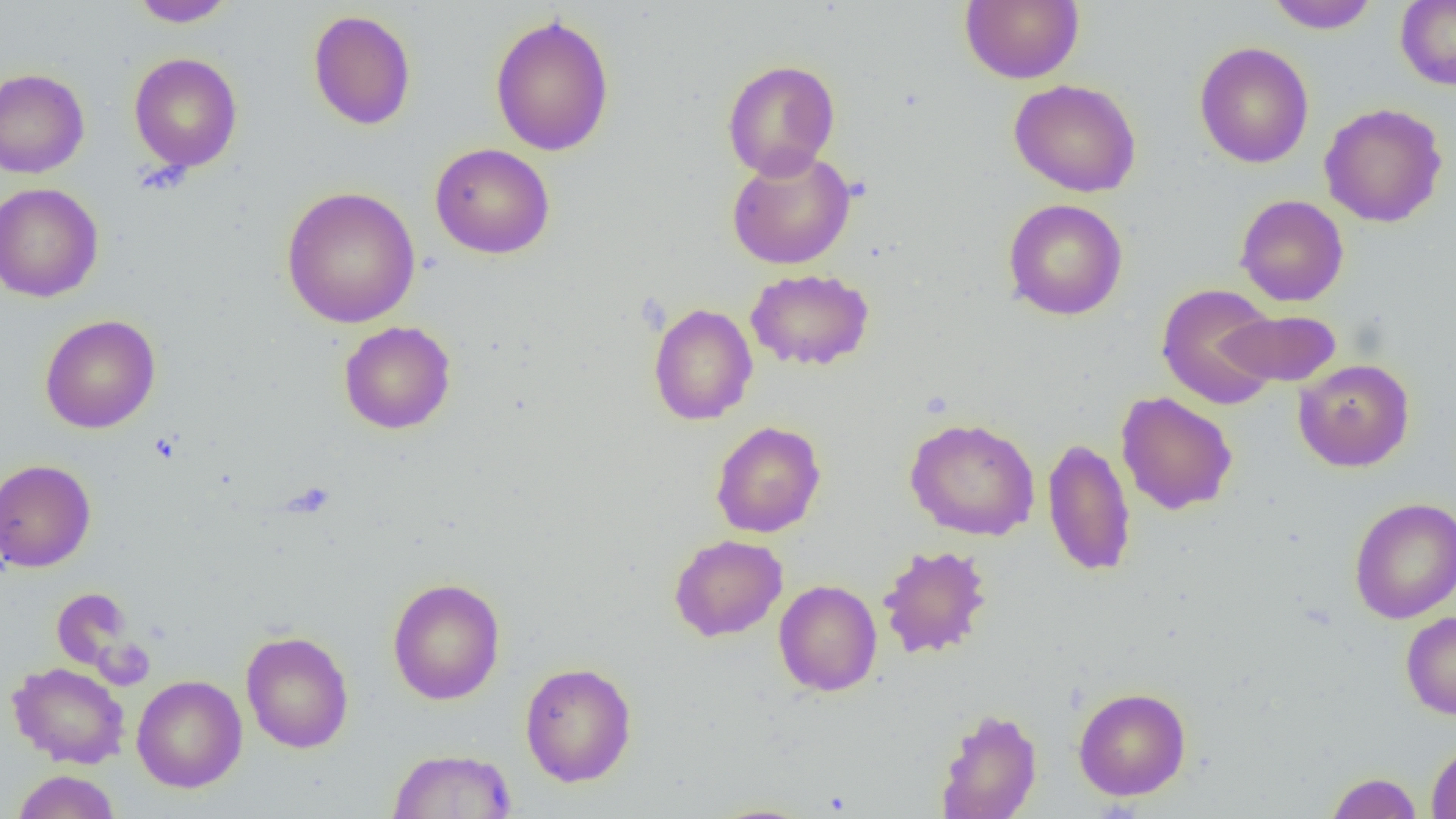

Summary:
  - Coordinate format: approximate bounding boxes as [x1, y1, x2, y2] in pixels
  - Uninfected red blood cell locations: [130, 0, 237, 27], [959, 0, 1083, 84], [1265, 0, 1380, 33], [1395, 0, 1456, 91], [308, 9, 416, 130], [489, 14, 615, 157], [1195, 41, 1314, 168], [129, 52, 243, 172], [722, 59, 840, 180], [0, 68, 90, 178], [1008, 78, 1142, 197], [1319, 102, 1449, 228], [430, 142, 555, 259], [726, 148, 856, 270], [0, 182, 104, 303], [281, 186, 421, 328], [1234, 194, 1349, 307], [1003, 198, 1128, 321], [745, 268, 874, 371], [1156, 283, 1282, 409], [648, 302, 758, 425], [1219, 308, 1341, 388], [40, 314, 160, 433], [339, 321, 456, 434], [1293, 358, 1415, 472], [1115, 391, 1238, 516], [904, 417, 1040, 541], [710, 420, 826, 538], [1042, 437, 1136, 577], [0, 459, 97, 573], [1349, 497, 1456, 624], [668, 534, 787, 642], [878, 545, 993, 659], [387, 577, 506, 705], [773, 580, 883, 696], [52, 588, 136, 673], [1400, 611, 1456, 719], [241, 631, 354, 754], [8, 661, 130, 768], [520, 662, 637, 787], [132, 675, 247, 793], [1073, 686, 1192, 801], [934, 707, 1042, 819], [1426, 740, 1456, 819], [386, 748, 517, 819], [12, 770, 120, 819], [1325, 772, 1423, 818], [701, 802, 821, 819]
  - Slide-level diagnosis: no evidence of blood parasites
  - Preparation: thin blood smear
  - Magnification: 1000x
  - Modality: optical microscopy
  - Field of view: one of a larger specimen
  - Image size: 1456×819 pixels